Give the position of every Plasmodium parasite visible.
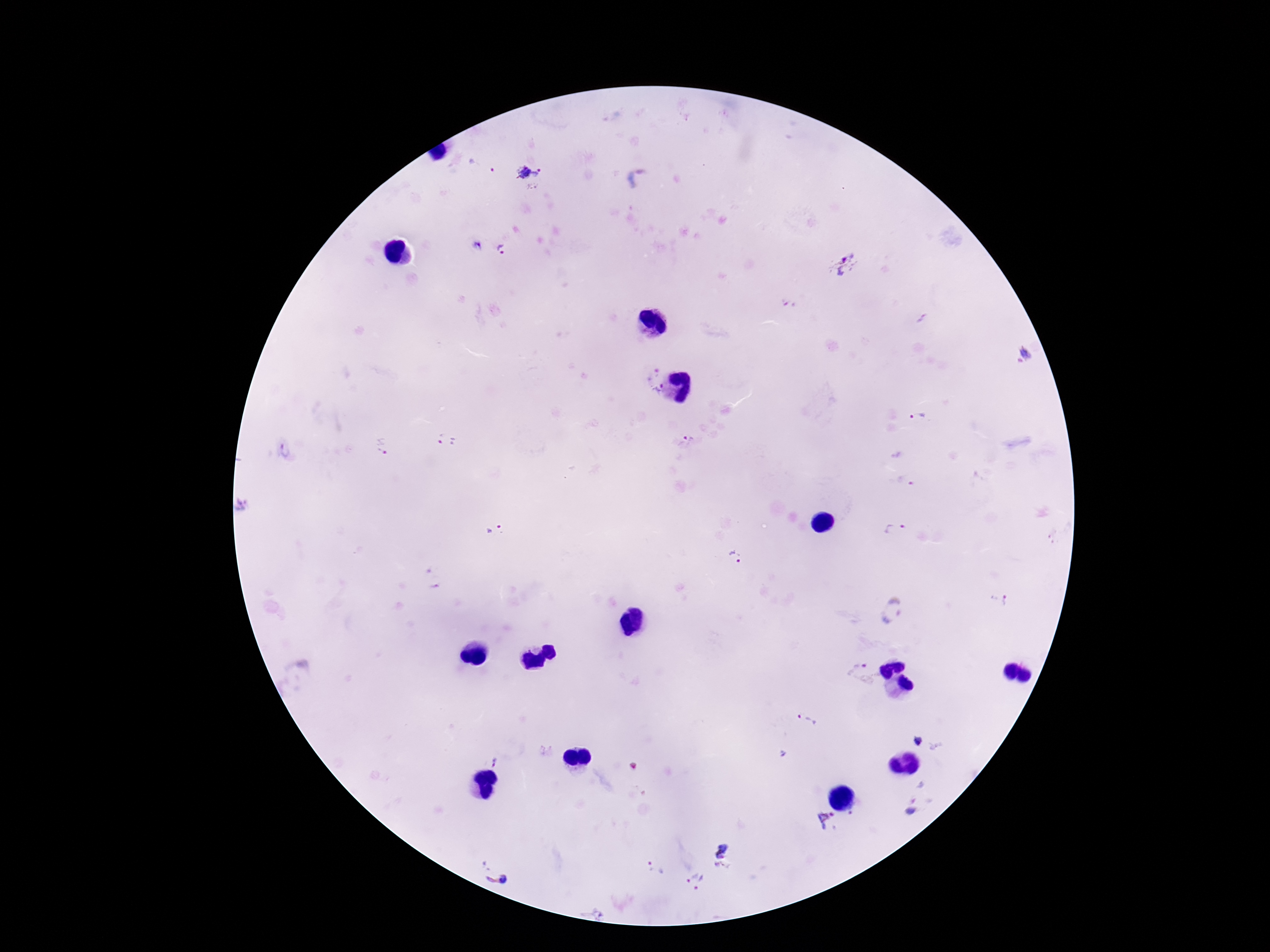

Approximate centers as [x, y] in pixels.
Plasmodium parasites: [528, 173], [640, 179], [478, 249], [501, 249], [846, 264], [1024, 357], [650, 371], [655, 392], [918, 416], [688, 439], [447, 442], [382, 446], [284, 452], [905, 481], [243, 507], [496, 530], [895, 530], [734, 557], [998, 600], [890, 610], [864, 674], [807, 719], [918, 740], [497, 762], [914, 806], [827, 818], [726, 855], [496, 867], [655, 870], [695, 881], [596, 910].

capture = smartphone camera through the microscope eyepiece
field of view = one from this slide
patient malaria status = positive
image size = 1270×952 pixels
preparation = thick peripheral-blood smear
stain = Giemsa
magnification = 100x